Classify this cell by malaria status.
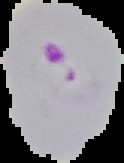
It is parasitized.

Summary:
  - Image type: segmented cell region on a black background
  - Image size: 124×163 pixels
  - Preparation: thin blood film